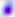 Photomicrograph. Toxoplasma gondii is seen. Captured at 400x magnification.